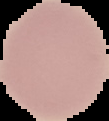

Summary:
  - Image type: cell region segmented out of the field of view; surrounding area masked to black
  - Result: no malaria parasites detected
  - Image size: 109×121 pixels
  - Preparation: thin blood smear